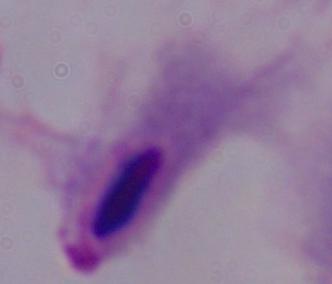 Micrograph. A trichomonad is shown. Captured at 1000x magnification.